Give the extent of the Plasmodium falciparum parasites you find, grouped by life-cycle stage — ring form, trophozoite, schizont, or gametocyte.
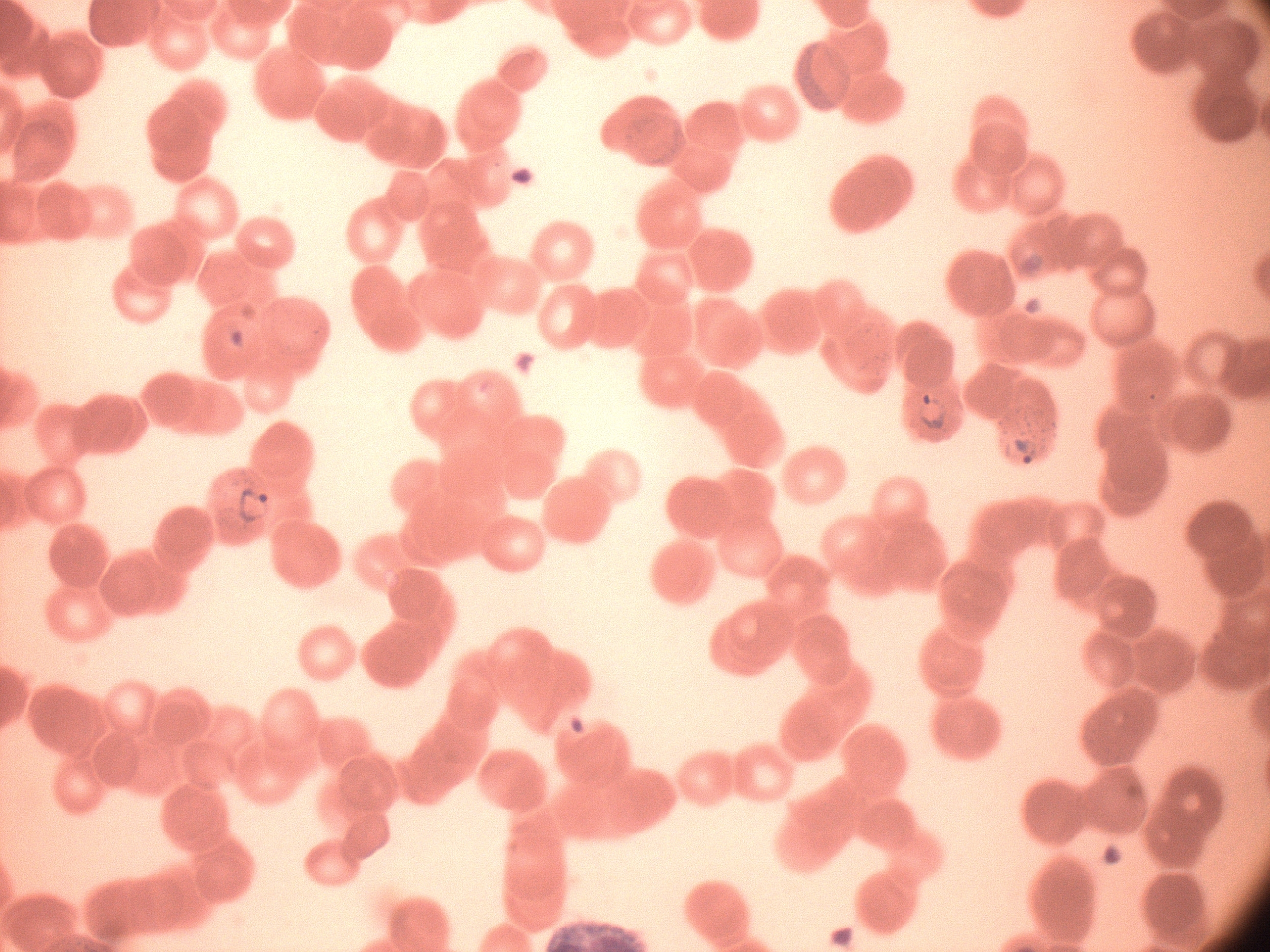

Approximate bounding boxes as (x1, y1, x2, y2) in pixels, from the source annotation, which is not necessarily exhaustive.
Ring forms: (916, 390, 952, 435), (1003, 417, 1052, 473), (229, 482, 277, 529).

{
  "magnification": "100x",
  "microscope": "Leica DM2000 with built-in camera",
  "preparation": "thin blood smear",
  "species": "Plasmodium falciparum",
  "image_size": "1270×952 pixels",
  "stain": "Giemsa",
  "field_of_view": "single"
}